State which parasite is depicted.
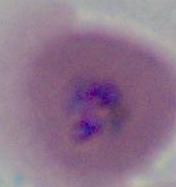

Plasmodium.

Micrograph. Captured at either 400x or 1000x magnification.